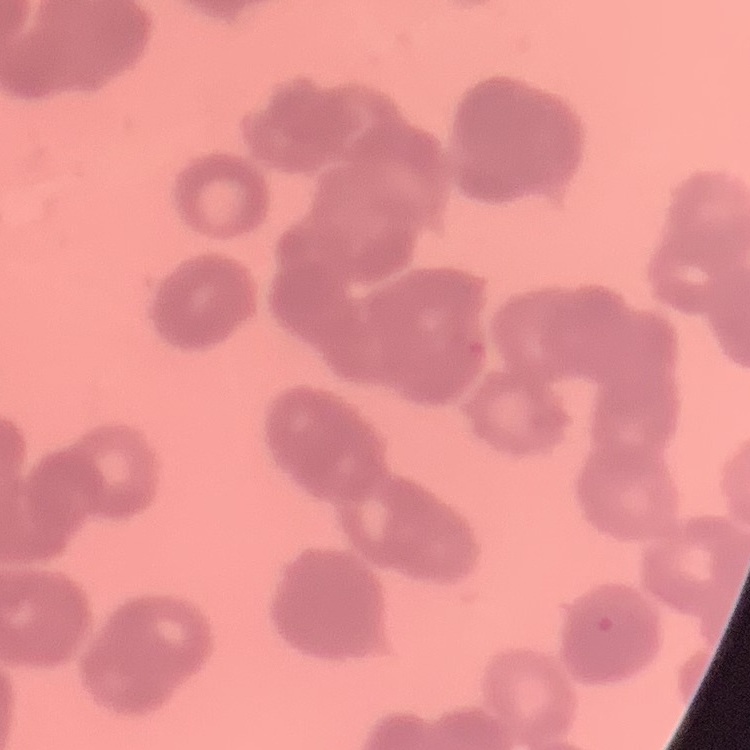

erythrocyte morphology = rouleaux formation
preparation = thin blood smear
image type = one tile cut from a larger photomicrograph
stain = Field's or Giemsa